State which parasite is depicted.
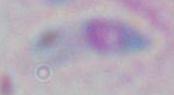

Toxoplasma gondii.

Summary:
  - Magnification: 1000x
  - Modality: photomicrograph